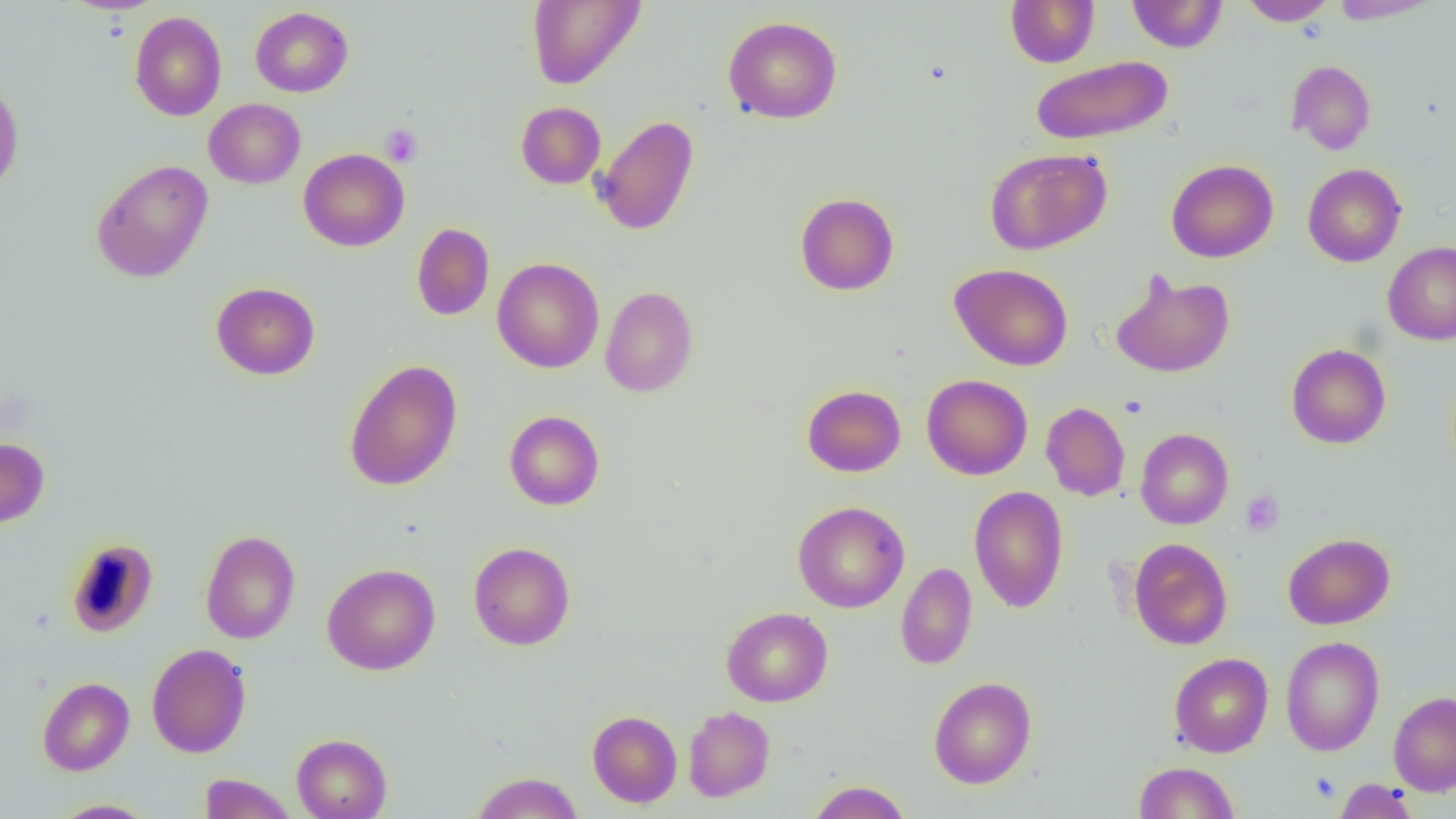

Summary:
  - Coordinate format: approximate bounding boxes as named x1/y1/x2/y2 corners in pixels
  - Uninfected red blood cell locations: (x1=61, y1=0, x2=166, y2=15), (x1=526, y1=0, x2=646, y2=89), (x1=1005, y1=0, x2=1099, y2=67), (x1=1127, y1=0, x2=1227, y2=52), (x1=1238, y1=0, x2=1337, y2=25), (x1=1329, y1=0, x2=1441, y2=24), (x1=250, y1=6, x2=353, y2=97), (x1=129, y1=11, x2=227, y2=121), (x1=723, y1=16, x2=842, y2=124), (x1=1031, y1=55, x2=1173, y2=145), (x1=1286, y1=60, x2=1376, y2=155), (x1=0, y1=81, x2=24, y2=196), (x1=204, y1=98, x2=305, y2=188), (x1=516, y1=102, x2=606, y2=189), (x1=592, y1=115, x2=699, y2=236), (x1=984, y1=147, x2=1112, y2=255), (x1=298, y1=148, x2=410, y2=251), (x1=91, y1=159, x2=214, y2=283), (x1=1166, y1=159, x2=1278, y2=263), (x1=1303, y1=163, x2=1406, y2=267), (x1=794, y1=192, x2=900, y2=296), (x1=412, y1=222, x2=495, y2=320), (x1=1383, y1=241, x2=1456, y2=345), (x1=492, y1=257, x2=605, y2=373), (x1=950, y1=263, x2=1073, y2=371), (x1=1110, y1=270, x2=1235, y2=379), (x1=211, y1=282, x2=320, y2=380), (x1=600, y1=286, x2=698, y2=397), (x1=1286, y1=344, x2=1391, y2=449), (x1=344, y1=359, x2=462, y2=491), (x1=921, y1=374, x2=1032, y2=480), (x1=802, y1=384, x2=906, y2=477), (x1=1041, y1=401, x2=1131, y2=501), (x1=504, y1=410, x2=605, y2=510), (x1=1135, y1=428, x2=1233, y2=529), (x1=0, y1=436, x2=50, y2=529), (x1=969, y1=485, x2=1069, y2=613), (x1=792, y1=501, x2=909, y2=613), (x1=200, y1=529, x2=300, y2=644), (x1=1283, y1=533, x2=1395, y2=629), (x1=65, y1=538, x2=159, y2=637), (x1=1129, y1=538, x2=1233, y2=650), (x1=468, y1=542, x2=575, y2=650), (x1=896, y1=562, x2=977, y2=670), (x1=322, y1=563, x2=441, y2=675), (x1=721, y1=607, x2=833, y2=706), (x1=1280, y1=635, x2=1385, y2=756), (x1=147, y1=643, x2=252, y2=758), (x1=1168, y1=653, x2=1273, y2=757), (x1=928, y1=676, x2=1037, y2=789), (x1=37, y1=677, x2=134, y2=775), (x1=1388, y1=690, x2=1456, y2=796), (x1=683, y1=706, x2=775, y2=802), (x1=587, y1=710, x2=682, y2=808), (x1=292, y1=733, x2=392, y2=819), (x1=1133, y1=761, x2=1239, y2=818), (x1=470, y1=771, x2=584, y2=818), (x1=198, y1=773, x2=297, y2=819), (x1=1334, y1=778, x2=1418, y2=819), (x1=806, y1=780, x2=912, y2=819), (x1=50, y1=799, x2=157, y2=818)
  - Platelet locations: (x1=380, y1=124, x2=422, y2=167), (x1=1241, y1=491, x2=1284, y2=536), (x1=1310, y1=772, x2=1340, y2=802)
  - Slide-level diagnosis: no evidence of blood parasites
  - Modality: light microscopy
  - Preparation: thin blood smear
  - Magnification: 1000x
  - Image size: 1456×819 pixels
  - Field of view: one of a larger specimen